Draw a bounding box around every parasitised red blood cell, every trophozoite, every gametocyte, every leukocyte, and every artifact (platelet-like body, stain precipitate, or debris).
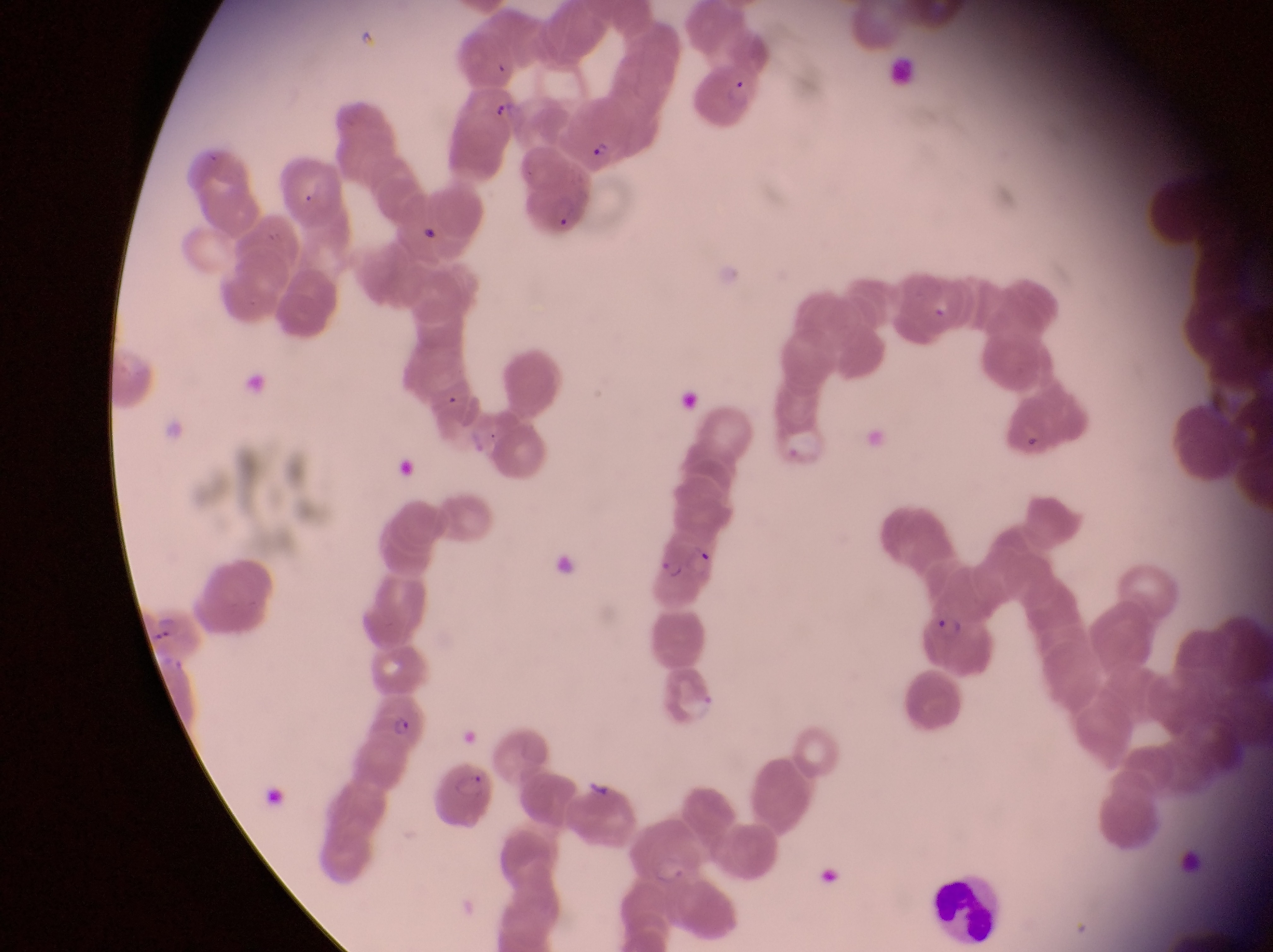

Approximate bounding boxes as {left, top, right, bottom} in pixels.
Parasitised red blood cells: {694, 63, 757, 125}, {556, 104, 631, 167}, {516, 164, 599, 238}, {1006, 392, 1098, 464}, {654, 537, 724, 614}, {145, 604, 202, 657}, {919, 610, 994, 687}, {372, 687, 434, 749}, {432, 761, 501, 831}.
Leukocytes: {926, 866, 1000, 946}.
Artifacts (platelet-like body, stain precipitate, or debris): {552, 549, 580, 580}.

country = Uganda
magnification = 1000x
preparation = thin blood film
capture = smartphone photograph through the eyepiece of an Olympus CX-23 microscope
field of view = single
image size = 1273×952 pixels